Identify the blood parasite species.
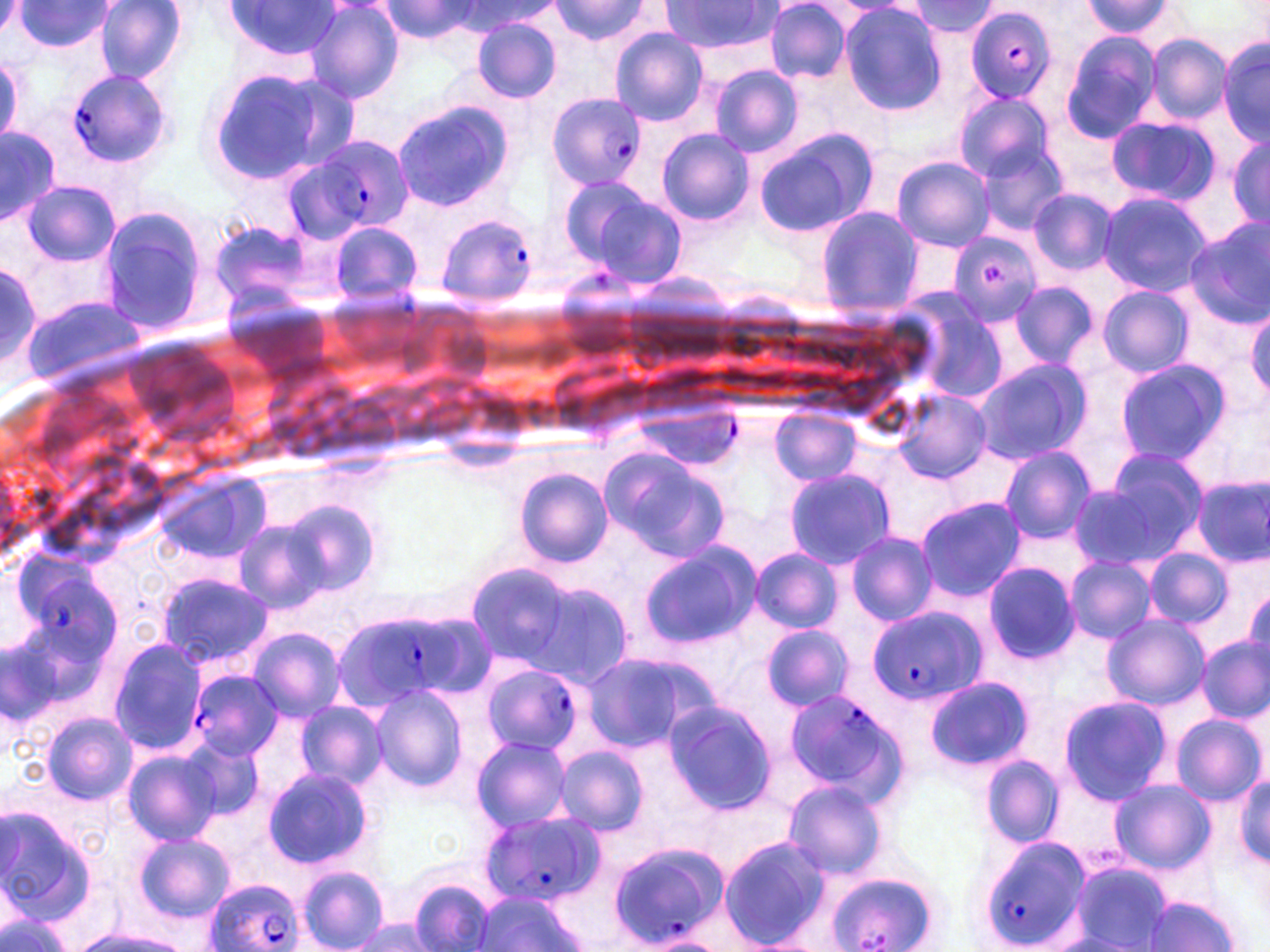
Plasmodium falciparum.

modality: light microscopy
plasmodium_falciparum_infected_red_blood_cell_locations: 'approximate bounding boxes as (x1, y1, x2, y2) in pixels: (965, 7, 1058, 105), (66, 71, 170, 170), (547, 92, 645, 189), (293, 134, 415, 241), (434, 211, 538, 305), (947, 231, 1042, 326), (39, 576, 119, 665), (870, 607, 987, 707), (365, 618, 465, 698), (482, 662, 580, 755), (188, 669, 283, 762), (787, 689, 904, 798), (479, 811, 604, 907), (979, 834, 1093, 950), (607, 841, 729, 948), (826, 871, 934, 951), (203, 878, 304, 952)'
uninfected_red_blood_cell_locations: 'approximate bounding boxes as (x1, y1, x2, y2) in pixels: (0, 0, 29, 37), (459, 0, 562, 33), (661, 0, 775, 53), (14, 1, 115, 50), (548, 1, 655, 44), (765, 1, 851, 81), (910, 1, 1001, 37), (1078, 1, 1177, 40), (95, 2, 186, 84), (223, 2, 341, 60), (305, 2, 406, 106), (376, 2, 485, 43), (839, 3, 947, 114), (471, 19, 561, 103), (609, 27, 709, 126), (1059, 31, 1164, 144), (1145, 33, 1231, 125), (1217, 34, 1270, 145), (0, 55, 24, 146), (711, 65, 801, 158), (206, 66, 342, 185), (953, 91, 1056, 182), (390, 100, 515, 210), (1105, 116, 1219, 206), (1, 125, 60, 227), (657, 129, 753, 226), (753, 129, 877, 237), (1225, 130, 1270, 233), (973, 138, 1071, 235), (892, 156, 994, 250), (558, 176, 654, 265), (21, 180, 120, 267), (582, 191, 688, 290), (1029, 191, 1116, 274), (1097, 191, 1212, 296), (95, 205, 211, 337), (814, 206, 924, 319), (211, 218, 315, 312), (1185, 219, 1270, 327), (327, 221, 423, 305), (0, 263, 52, 387), (1011, 281, 1099, 369), (1098, 286, 1195, 378), (21, 293, 148, 393), (906, 302, 1008, 403), (1246, 304, 1270, 400), (971, 359, 1090, 465), (1114, 359, 1230, 466), (894, 388, 992, 484), (639, 409, 739, 469), (770, 410, 863, 485), (597, 443, 727, 561), (997, 444, 1096, 543), (1101, 445, 1209, 555), (783, 468, 895, 569), (517, 469, 611, 565), (159, 472, 267, 567), (1192, 474, 1270, 568), (1067, 485, 1178, 570), (914, 496, 1025, 602), (284, 501, 381, 598), (232, 519, 331, 615), (845, 531, 939, 626), (640, 542, 761, 648), (751, 547, 842, 633), (1143, 547, 1232, 629), (1064, 556, 1157, 643), (469, 564, 571, 667), (981, 564, 1080, 662), (157, 572, 270, 668), (528, 581, 636, 688), (1243, 590, 1270, 668), (1101, 614, 1210, 711), (761, 625, 853, 712), (249, 628, 345, 720), (1198, 636, 1269, 722), (107, 638, 208, 754), (579, 652, 712, 754), (925, 676, 1031, 771), (369, 683, 468, 791), (1058, 695, 1172, 804), (294, 700, 388, 792), (662, 700, 775, 813), (41, 710, 137, 805), (1171, 713, 1265, 805), (181, 734, 263, 823), (470, 735, 573, 833), (553, 746, 650, 835), (121, 750, 222, 845), (982, 756, 1064, 846), (262, 766, 375, 869), (1234, 774, 1269, 867), (1108, 780, 1214, 875), (783, 781, 886, 881), (0, 805, 98, 927), (135, 833, 234, 922), (720, 836, 831, 950), (1069, 862, 1172, 950), (297, 865, 389, 952), (408, 876, 498, 952), (474, 890, 584, 952), (1142, 896, 1241, 951), (0, 903, 80, 952), (347, 918, 439, 951), (75, 931, 188, 952), (640, 933, 726, 952), (1049, 934, 1142, 952)'
image_size: 1270×952 pixels
field_of_view: single
preparation: thin blood smear
magnification: 1000x
stain: May-Grünwald-Giemsa